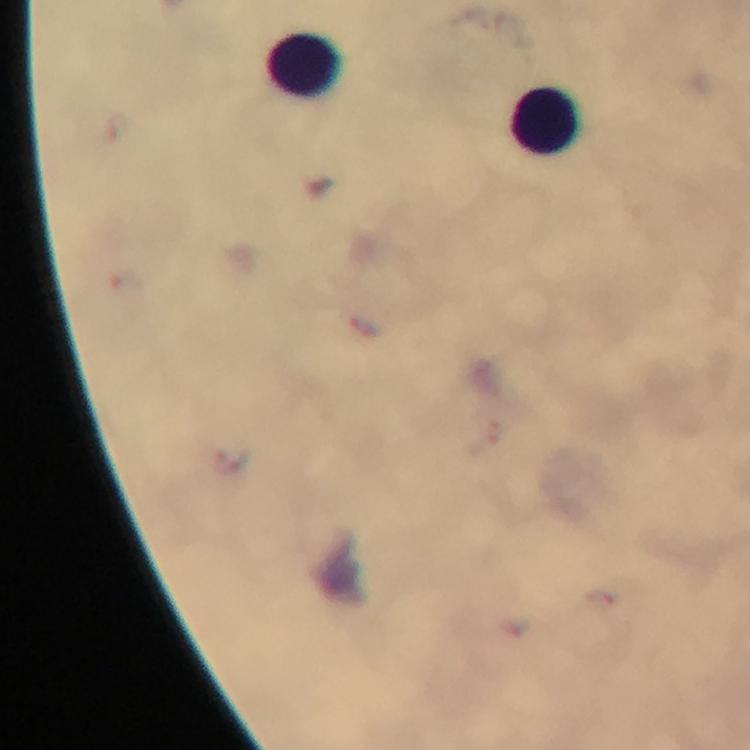

Approximate centers as {x, y} in pixels.
Summary:
  - Leukocyte locations: {308, 66}, {548, 120}
  - Plasmodium parasites: none detected
  - Image size: 750×750 pixels
  - Magnification: 100x
  - Cropped from: a single field of view
  - Immersion oil: used
  - Stain: Giemsa
  - Preparation: thick blood smear
  - Capture: smartphone camera through the microscope
  - Context: from a malaria diagnostic workup